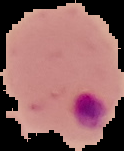

preparation = thin blood film
result = malaria parasites identified
image type = segmented cell region on a black background
image size = 124×151 pixels